Assess this cell for malaria.
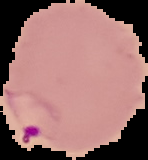

Parasitized.

The area outside the segmented cell region is set to black. From a thin blood film. Image is 148×160 pixels.